Assess this cell for malaria.
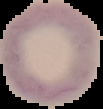
It is uninfected.

Image is 103×109 pixels. The area outside the segmented cell region is set to black. From a thin blood film.